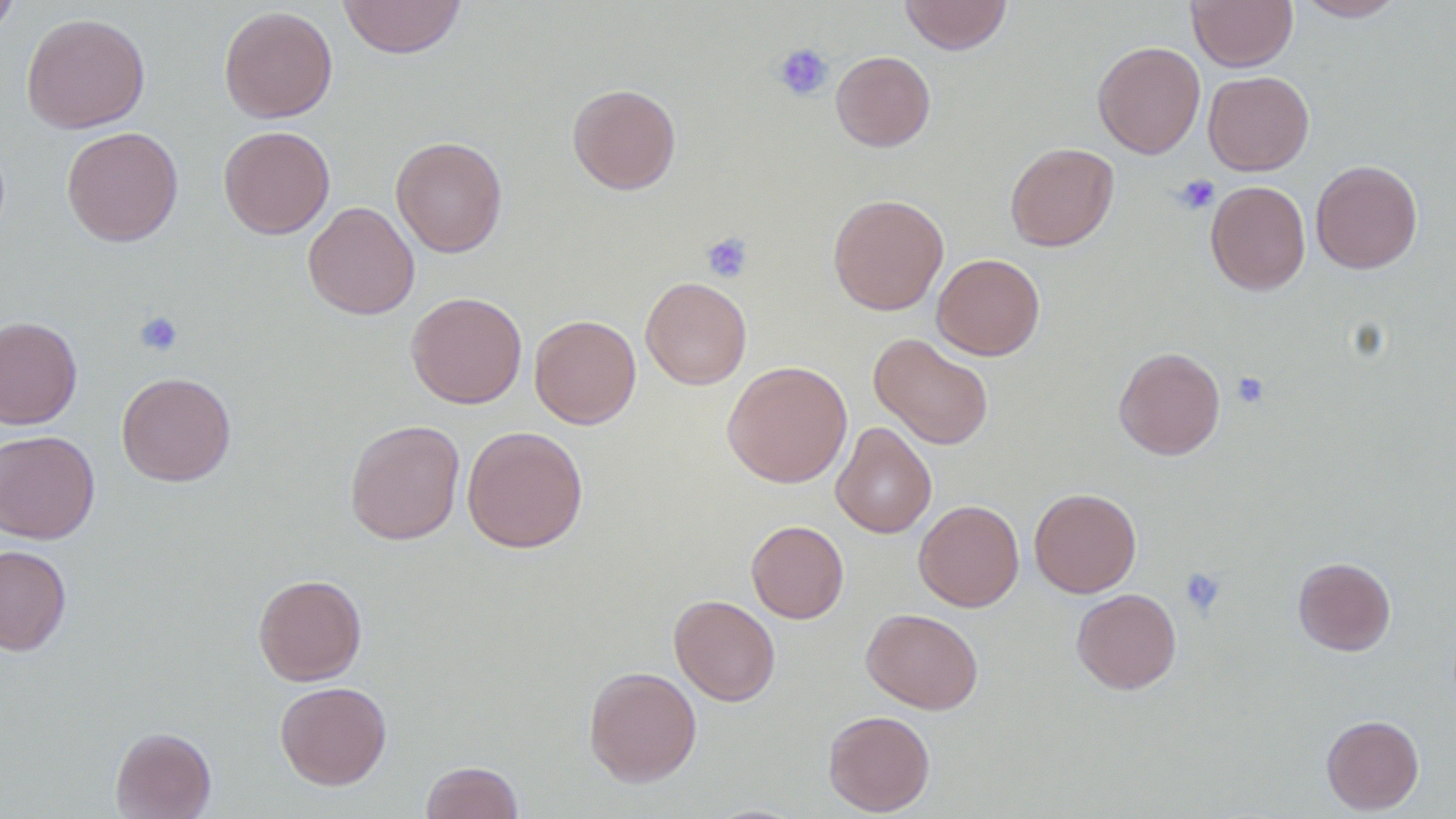

Summary:
  - Coordinate format: approximate bounding boxes as [x1, y1, x2, y2] in pixels
  - Uninfected red blood cell locations: [337, 0, 467, 59], [899, 0, 1013, 55], [1187, 0, 1298, 72], [1294, 0, 1410, 21], [0, 1, 20, 39], [219, 6, 338, 123], [21, 13, 150, 133], [1092, 41, 1205, 158], [831, 50, 935, 151], [1203, 70, 1314, 176], [567, 83, 681, 195], [218, 124, 335, 239], [61, 126, 184, 247], [390, 135, 507, 257], [1005, 142, 1119, 251], [1310, 159, 1423, 274], [1206, 180, 1310, 295], [827, 193, 949, 315], [303, 201, 420, 319], [932, 253, 1045, 360], [640, 276, 752, 389], [406, 291, 527, 408], [529, 314, 641, 429], [0, 315, 83, 429], [869, 332, 994, 450], [1114, 346, 1225, 459], [722, 361, 852, 487], [116, 371, 236, 486], [345, 419, 465, 545], [831, 422, 937, 538], [461, 425, 588, 553], [0, 430, 100, 544], [1029, 488, 1142, 597], [914, 499, 1024, 612], [746, 519, 849, 623], [0, 544, 72, 656], [1293, 556, 1396, 655], [253, 573, 367, 686], [1071, 588, 1182, 694], [669, 594, 781, 706], [862, 608, 984, 714], [583, 666, 702, 786], [275, 681, 392, 790], [822, 710, 936, 816], [1321, 714, 1424, 815], [110, 726, 217, 818], [420, 761, 524, 819]
  - Platelet locations: [772, 43, 834, 101], [1174, 174, 1219, 214], [701, 231, 754, 283], [134, 311, 183, 357], [1232, 371, 1270, 409], [1179, 567, 1226, 617]
  - Slide-level diagnosis: negative for blood parasites
  - Preparation: thin blood smear
  - Field of view: one of a larger specimen
  - Image size: 1456×819 pixels
  - Magnification: 1000x
  - Modality: light microscopy